Describe the morphology of the erythrocytes.
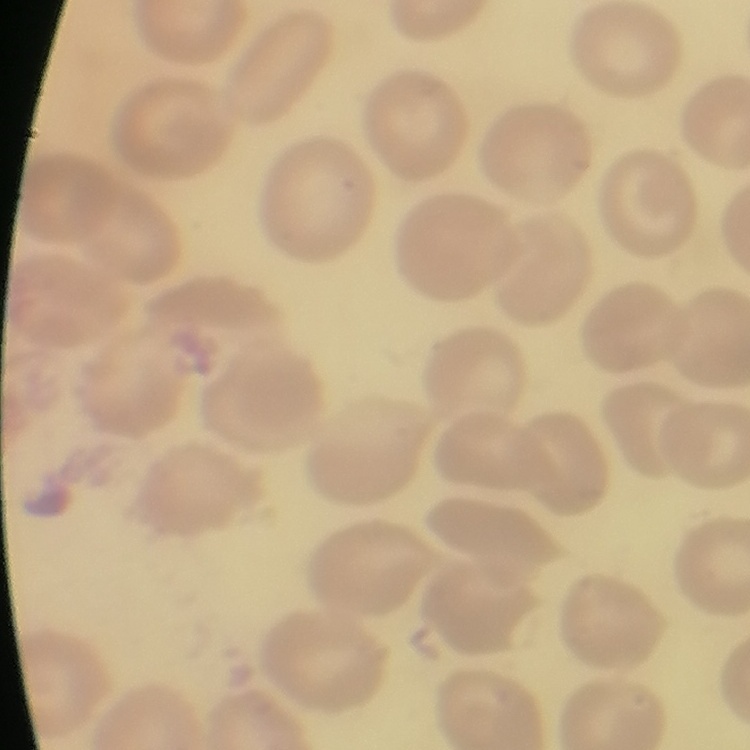

No rouleaux formation.

Square crop of a larger photomicrograph. Thin blood smear. Stained with either Field's or Giemsa.